Identify the parasite.
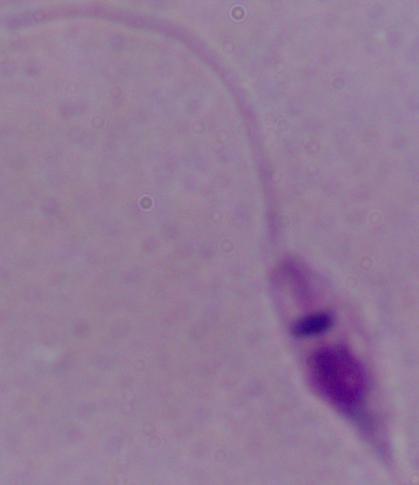

This is Leishmania.

Captured at 1000x magnification. Photomicrograph.